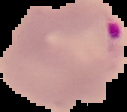

Summary:
  - Image size: 127×112 pixels
  - Result: malaria parasites detected
  - Image type: cell region segmented out of the field of view; surrounding area masked to black
  - Preparation: thin blood smear